Classify this cell by malaria status.
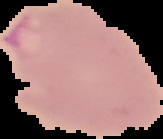
It is parasitized.

Summary:
  - Preparation: thin blood film
  - Image size: 163×139 pixels
  - Image type: segmented cell region on a black background